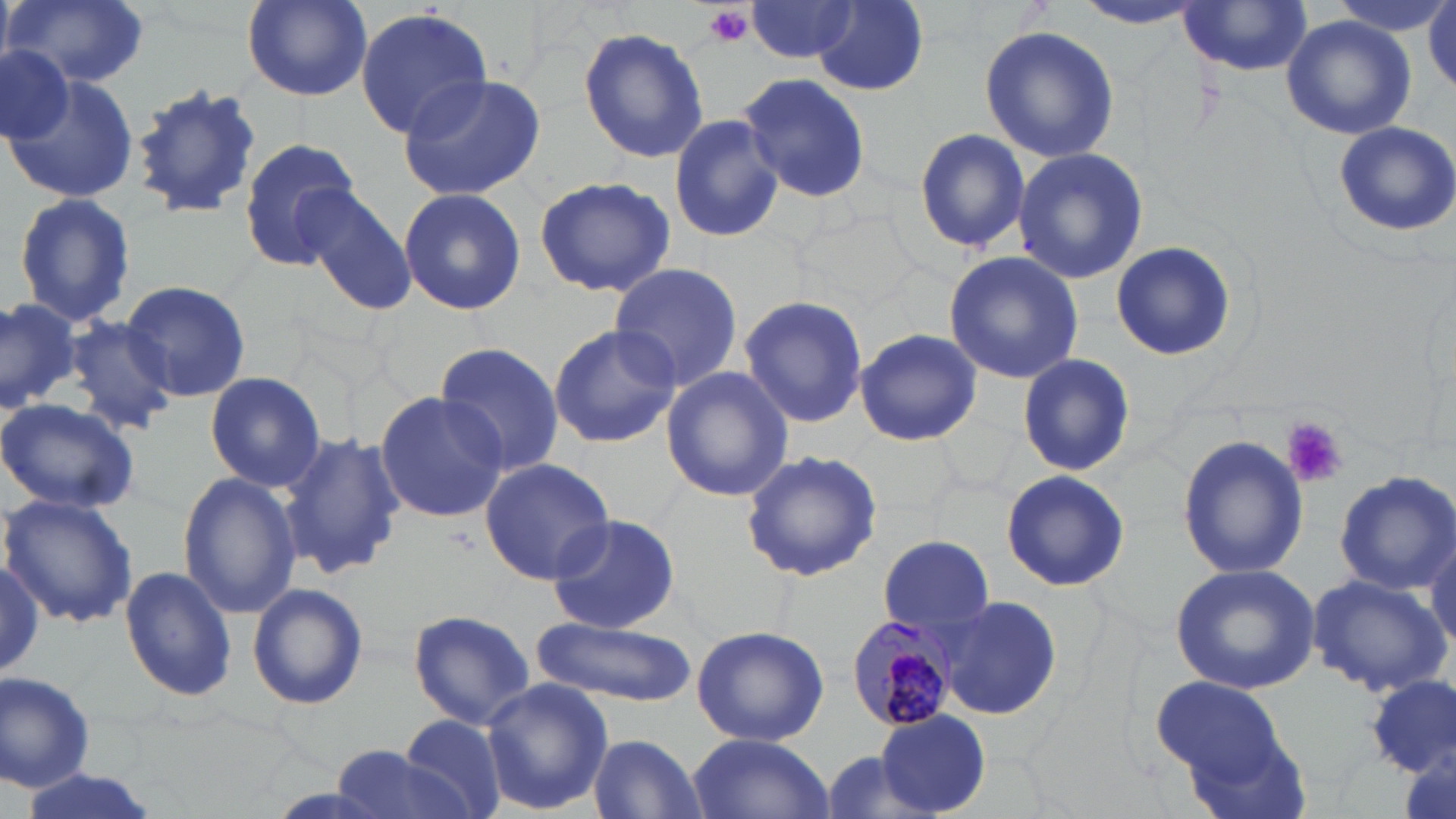
Approximate bounding boxes as (x1, y1, x2, y2) in pixels. Uninfected red blood cell locations: (6, 0, 150, 88), (240, 0, 374, 102), (1078, 1, 1208, 33), (1178, 2, 1316, 77), (1427, 2, 1456, 96), (745, 3, 862, 63), (807, 3, 932, 97), (355, 8, 493, 137), (1281, 17, 1416, 139), (980, 23, 1118, 162), (579, 26, 709, 164), (0, 45, 73, 142), (4, 68, 142, 205), (738, 72, 872, 204), (397, 73, 548, 202), (127, 84, 264, 221), (668, 115, 783, 245), (1332, 121, 1456, 237), (915, 127, 1030, 252), (238, 138, 363, 268), (1012, 146, 1149, 284), (532, 175, 676, 298), (293, 183, 418, 315), (398, 187, 529, 315), (10, 193, 138, 329), (1109, 241, 1236, 361), (943, 251, 1084, 383), (609, 262, 743, 393), (118, 279, 253, 401), (0, 294, 80, 414), (739, 296, 870, 429), (60, 313, 179, 435), (548, 322, 681, 448), (854, 326, 982, 447), (434, 344, 564, 477), (1019, 354, 1134, 476), (660, 366, 795, 503), (204, 370, 328, 492), (373, 390, 510, 523), (0, 396, 143, 517), (279, 431, 406, 582), (1178, 435, 1311, 581), (739, 450, 884, 581), (479, 457, 617, 583), (999, 467, 1130, 592), (1331, 470, 1456, 593), (176, 472, 302, 620), (2, 494, 137, 627), (543, 512, 683, 635), (1424, 526, 1456, 660), (879, 534, 994, 633), (0, 555, 52, 684), (1170, 563, 1322, 693), (121, 565, 238, 703), (1307, 574, 1450, 697), (247, 582, 369, 710), (938, 595, 1063, 721), (405, 607, 538, 729), (533, 615, 695, 708), (690, 624, 830, 748), (0, 668, 99, 791), (1365, 675, 1454, 775), (1151, 677, 1290, 780), (479, 678, 614, 814), (875, 710, 991, 815), (400, 714, 508, 819), (686, 733, 836, 819), (589, 734, 708, 818), (330, 742, 477, 819), (15, 770, 161, 819). Platelet locations: (700, 5, 754, 51), (1283, 419, 1348, 489). Plasmodium malariae-infected red blood cell locations: (841, 613, 967, 734). Slide-level diagnosis: Plasmodium malariae. Single field of view. Light microscopy. Captured at 1000x magnification. May-Grünwald-Giemsa stain. Thin blood film. Image is 1456×819 pixels.